Classify this cell by malaria status.
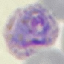

It is parasitized.

{
  "image_type": "automatically extracted cell patch, resized to 64 × 64 pixels",
  "stain": "Giemsa",
  "capture": "smartphone camera at the microscope eyepiece",
  "preparation": "thin blood smear"
}